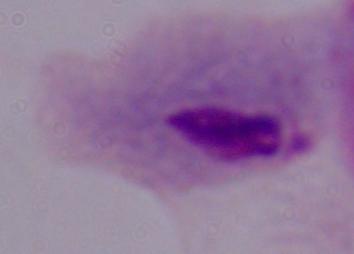

Captured at 1000x magnification. A trichomonad is shown. Micrograph.